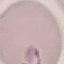
malaria status = parasitized
image type = automatically extracted cell patch, resized to 64 × 64 pixels
stain = Giemsa
capture = smartphone through the microscope eyepiece
preparation = thin blood film